Report the malaria status of this cell.
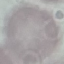
It is uninfected.

preparation: thin smear
capture: smartphone through the microscope eyepiece
image_type: cell patch, automatically extracted from a larger field of view and resized to 64 × 64 pixels
stain: Giemsa